Report the malaria status of this cell.
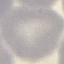
It is uninfected.

Summary:
  - Image type: cell patch, automatically extracted from a larger field of view and resized to 64 × 64 pixels
  - Stain: Giemsa
  - Capture: smartphone through the microscope eyepiece
  - Preparation: thin blood smear